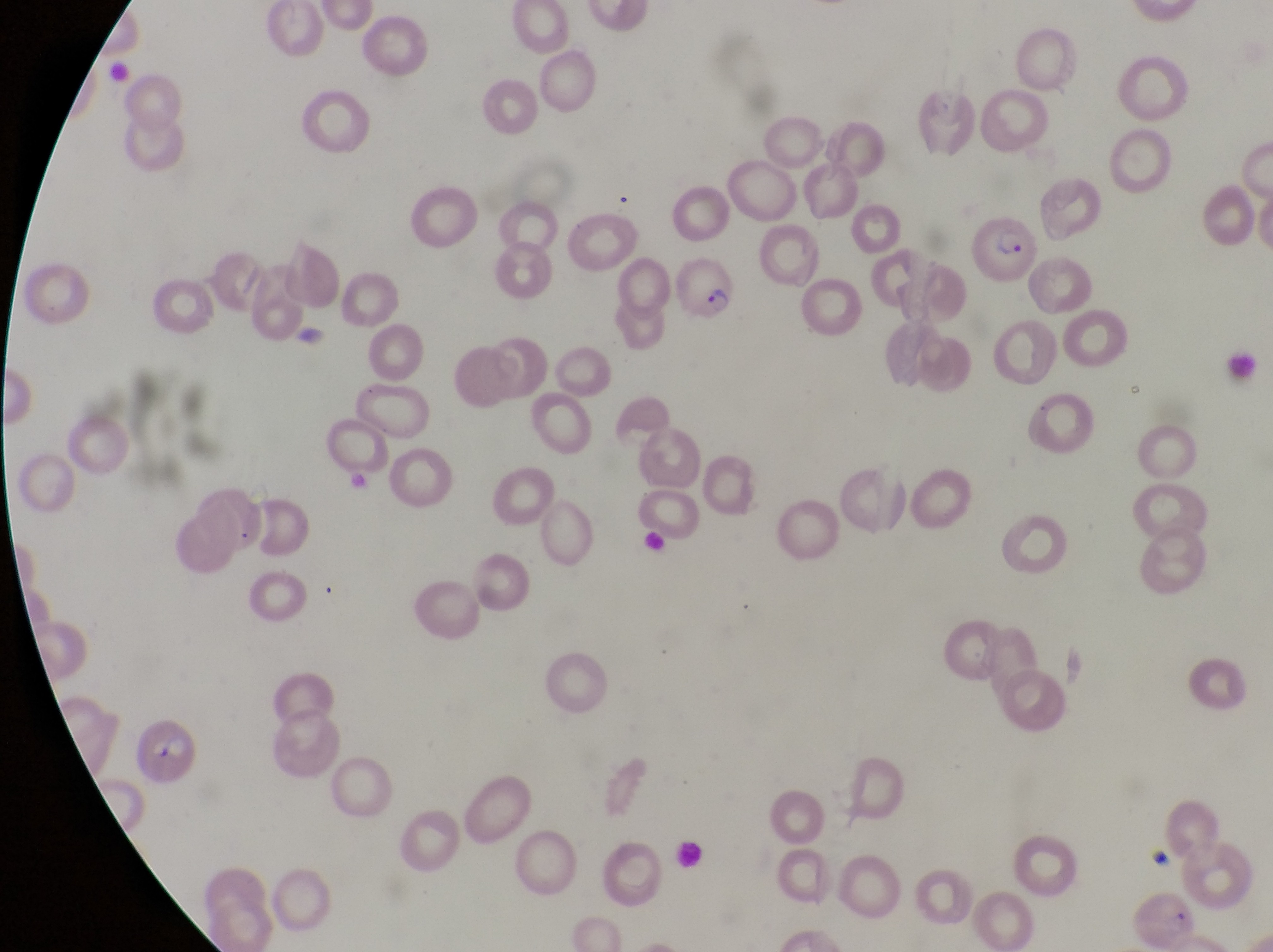

Approximate bounding boxes as left top right bottom in pixels.
Summary:
  - Leukocyte locations: 672 840 709 878
  - Artifact (platelet-like body, stain precipitate, or debris) locations: 1227 350 1264 392; 1127 378 1147 401; 347 469 380 504; 642 532 674 561; 1146 842 1174 865
  - Parasitised red blood cell locations: 966 205 1038 290; 677 255 739 327; 1138 886 1201 948
  - Field of view: single
  - Image size: 1273×952 pixels
  - Preparation: thin blood smear
  - Magnification: 1000x
  - Country: Uganda
  - Capture: smartphone photograph through the eyepiece of an Olympus CX-23 microscope